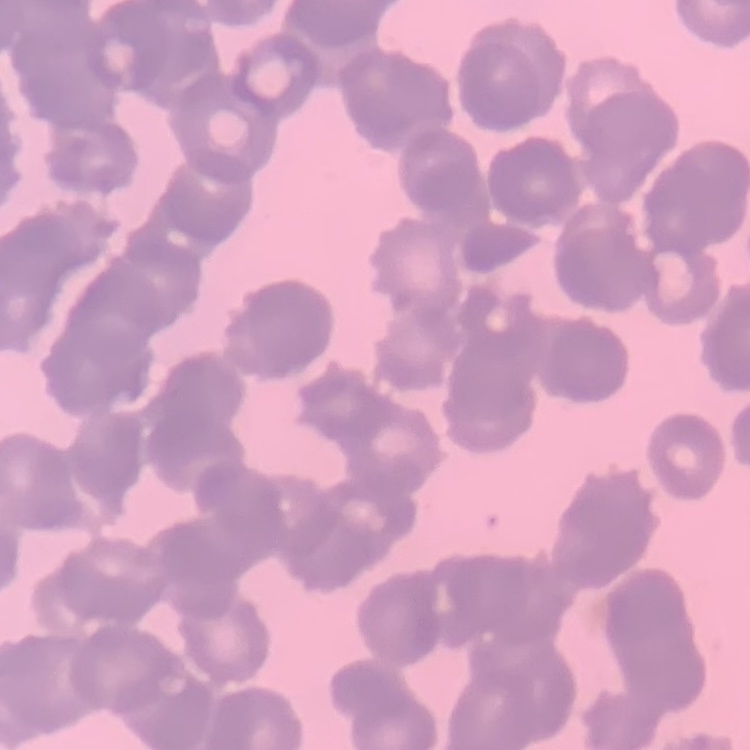
Summary:
  - Erythrocyte morphology: rouleaux formation
  - Image type: square crop of a larger photomicrograph
  - Stain: Field's or Giemsa
  - Preparation: thin peripheral smear